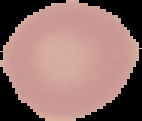

Summary:
  - Image type: cell region segmented out of the field of view; surrounding area masked to black
  - Image size: 142×121 pixels
  - Result: no Plasmodium parasites seen
  - Preparation: thin blood film